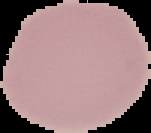

Malaria status: uninfected. Image is 151×133 pixels. From a thin blood smear. The area outside the segmented cell region is set to black.